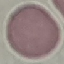
{
  "malaria_status": "uninfected",
  "image_type": "automatically extracted cell patch, resized to 64 × 64 pixels",
  "preparation": "thin blood film",
  "capture": "smartphone camera at the microscope eyepiece",
  "stain": "Giemsa"
}